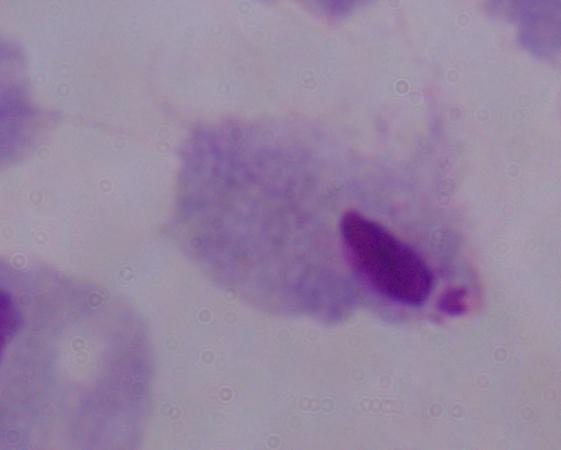
modality = micrograph
magnification = 1000x
identification = trichomonad